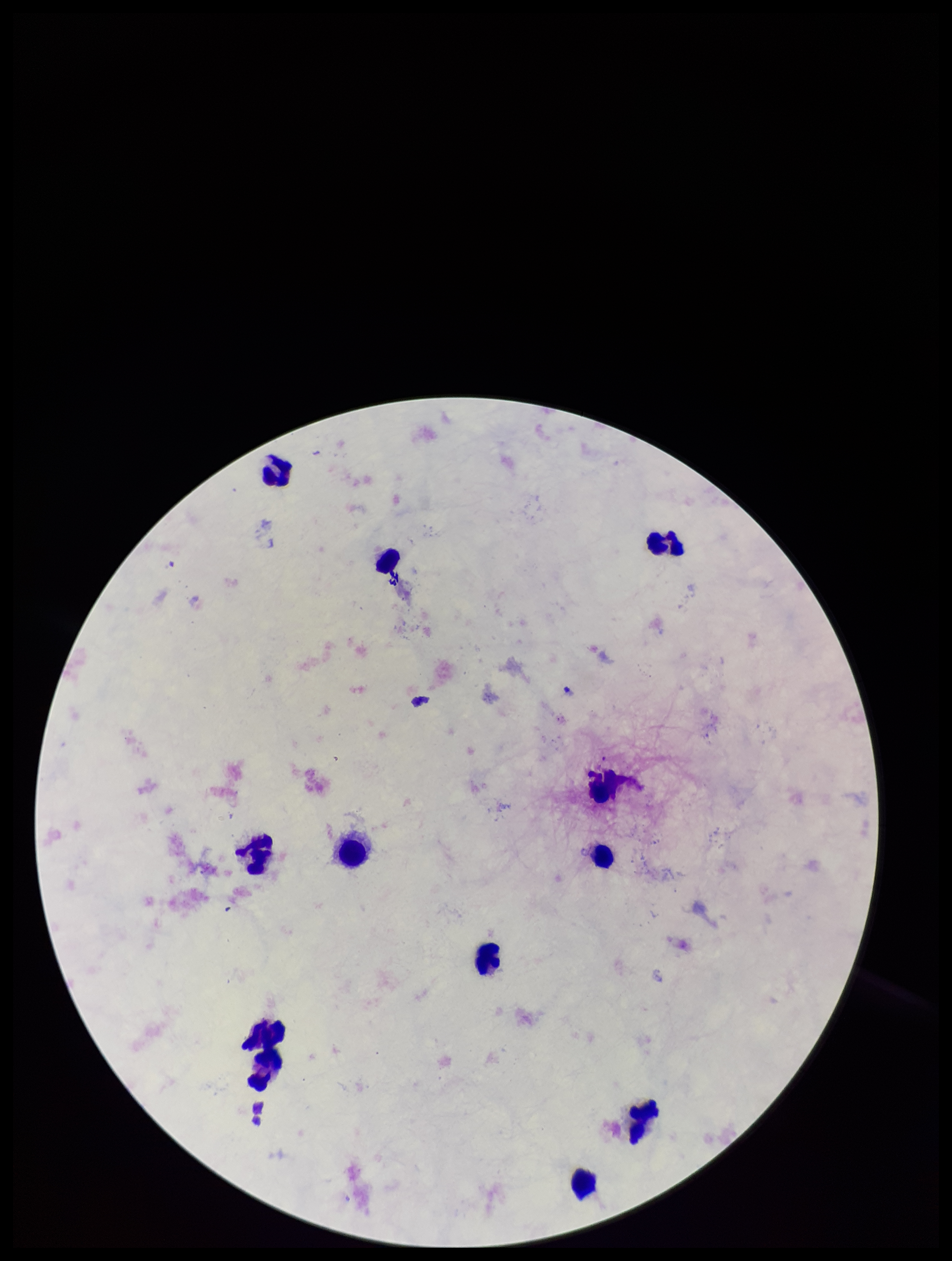
field of view = single
species reported for this patient = Plasmodium falciparum
leukocyte count = 12
image size = 952×1261 pixels
capture = smartphone photograph through the microscope eyepiece
preparation = thick
Plasmodium parasites = none seen
parasite count = 0
patient malaria status = positive
stain = Giemsa